Report the malaria status of this cell.
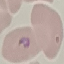

It is parasitized.

{
  "capture": "smartphone camera at the microscope eyepiece",
  "image_type": "automatically extracted cell patch, resized to 64 × 64 pixels",
  "stain": "Giemsa",
  "preparation": "thin blood smear"
}